Assess the morphology of the red blood cells.
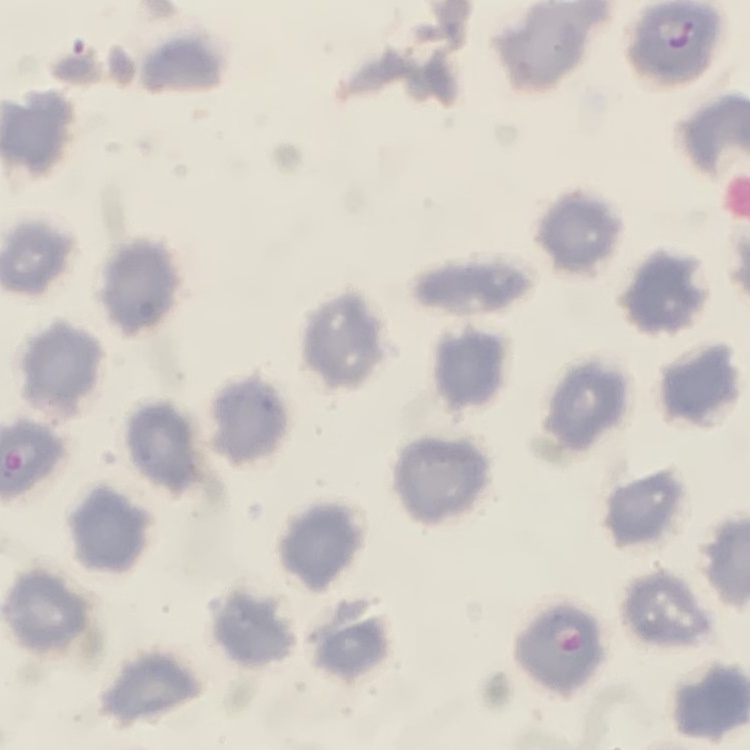
They show no rouleaux formation.

Thin blood smear. Stained with either Field's or Giemsa. Square crop of a larger photomicrograph.